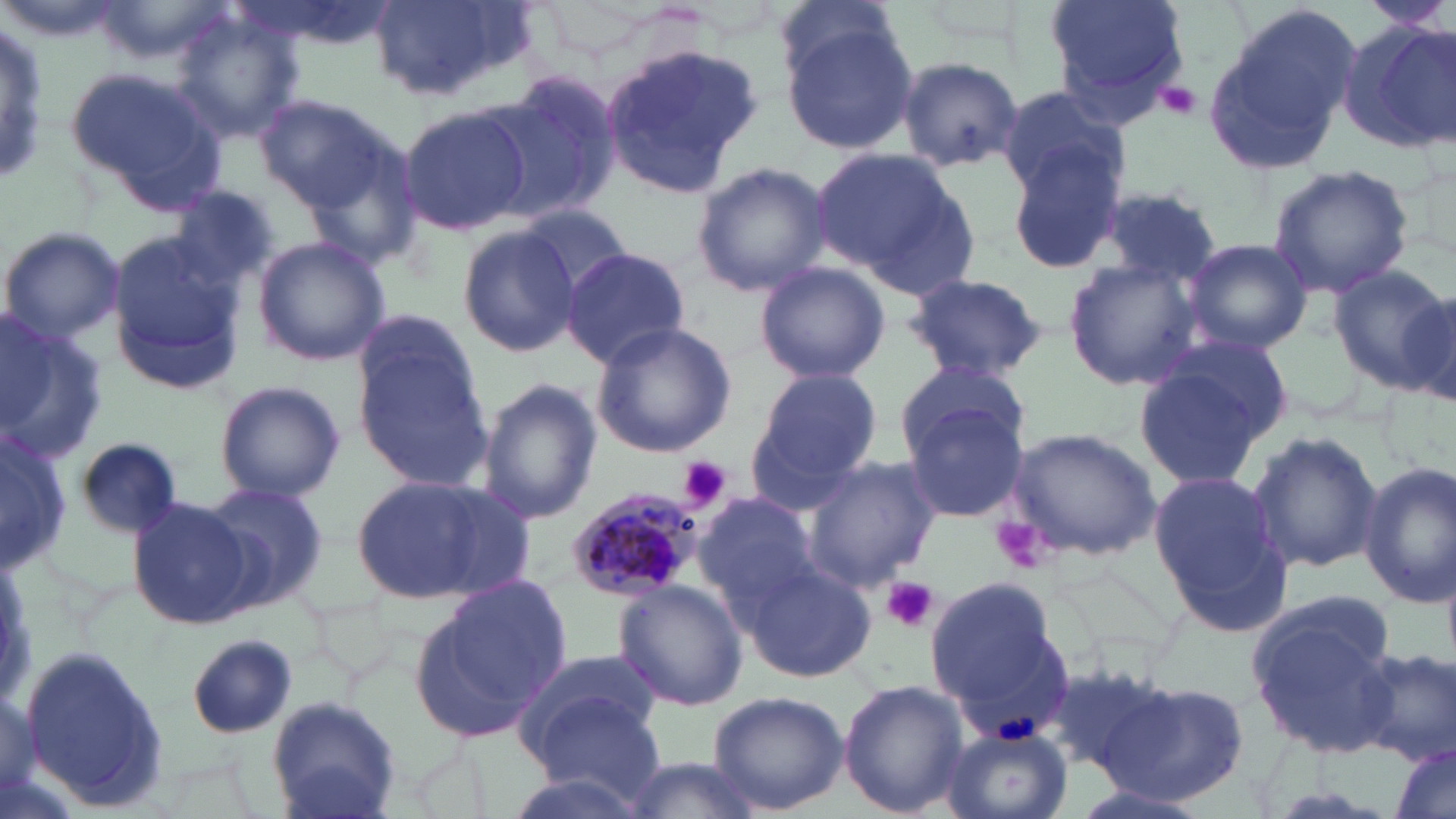 Approximate bounding boxes as [x1, y1, x2, y2] in pixels. Plasmodium malariae-infected red blood cell locations: [567, 485, 706, 604]. Platelet locations: [1155, 80, 1203, 121], [676, 456, 732, 513], [993, 516, 1050, 571], [879, 577, 938, 632]. Uninfected red blood cell locations: [1044, 0, 1191, 113], [1361, 0, 1456, 34], [94, 1, 227, 65], [366, 1, 532, 106], [1201, 5, 1359, 170], [169, 12, 304, 142], [779, 19, 919, 155], [1343, 19, 1454, 151], [598, 41, 764, 199], [895, 55, 1027, 174], [66, 63, 228, 209], [482, 72, 623, 225], [994, 83, 1129, 201], [252, 92, 395, 211], [399, 100, 532, 237], [1001, 144, 1127, 275], [812, 147, 968, 283], [691, 161, 831, 299], [1267, 163, 1413, 300], [164, 184, 285, 302], [1093, 185, 1224, 284], [514, 204, 632, 302], [0, 225, 122, 347], [107, 226, 249, 394], [457, 226, 582, 358], [252, 236, 391, 367], [1180, 237, 1312, 353], [560, 248, 692, 368], [1062, 260, 1206, 391], [754, 263, 890, 385], [1330, 264, 1453, 390], [903, 272, 1051, 382], [1400, 283, 1456, 410], [354, 303, 490, 436], [0, 306, 106, 469], [590, 321, 737, 457], [1132, 342, 1284, 490], [357, 350, 498, 491], [895, 359, 1027, 463], [746, 368, 882, 501], [476, 378, 602, 526], [216, 380, 344, 501], [902, 396, 1031, 524], [1005, 427, 1159, 561], [1246, 429, 1383, 575], [0, 430, 72, 567], [75, 438, 183, 539], [799, 456, 942, 592], [1358, 461, 1456, 608], [1146, 468, 1291, 636], [350, 472, 527, 605], [198, 481, 330, 611], [693, 491, 816, 609], [128, 497, 257, 629], [742, 560, 879, 681], [421, 573, 571, 729], [925, 577, 1068, 726], [614, 581, 746, 710], [1247, 599, 1400, 756], [187, 635, 297, 739], [20, 647, 169, 813], [1354, 648, 1455, 764], [516, 653, 662, 777], [1044, 659, 1177, 779], [1104, 678, 1250, 806], [838, 679, 968, 816], [707, 690, 848, 815], [265, 696, 402, 819], [940, 726, 1073, 819], [1387, 740, 1456, 819], [614, 752, 769, 819], [1064, 779, 1212, 819]. Slide-level diagnosis: Plasmodium malariae. Image is 1456×819 pixels. Thin blood smear. Single field of view. May-Grünwald-Giemsa-stained preparation. 1000x magnification. Light microscopy.